Name the parasite shown.
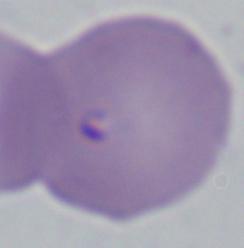
Babesia.

Summary:
  - Magnification: 1000x
  - Modality: micrograph